Identify the parasite.
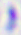
This is Toxoplasma gondii.

Micrograph. 400x magnification.